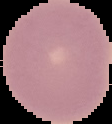
From a thin blood film. Malaria status: uninfected. Image is 112×124 pixels. Cell region segmented out of the field of view; the surrounding area is masked to black.